Report the malaria status of this cell.
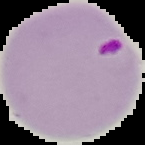
It is parasitized.

The area outside the segmented cell region is set to black. From a thin blood film. Image is 145×145 pixels.